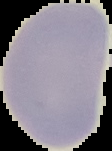
Result: no malaria parasites detected. Image is 112×151 pixels. From a thin blood film. The area outside the segmented cell region is set to black.